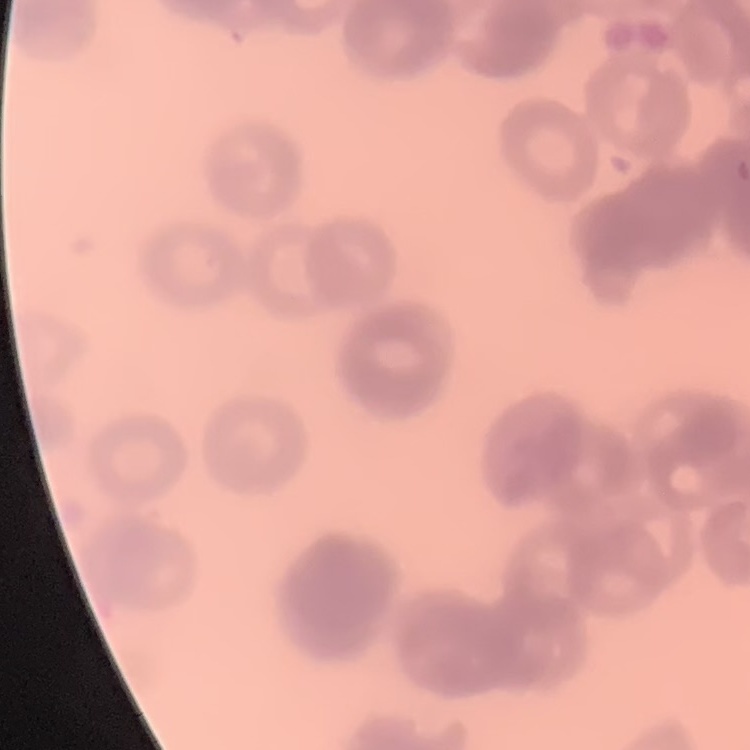
red blood cell morphology = rouleaux formation
stain = Field's or Giemsa
preparation = thin blood film
image type = one tile cut from a larger photomicrograph